Identify the parasite.
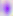

Toxoplasma gondii.

Summary:
  - Modality: micrograph
  - Magnification: 400x